Point out malaria parasites and leukocytes.
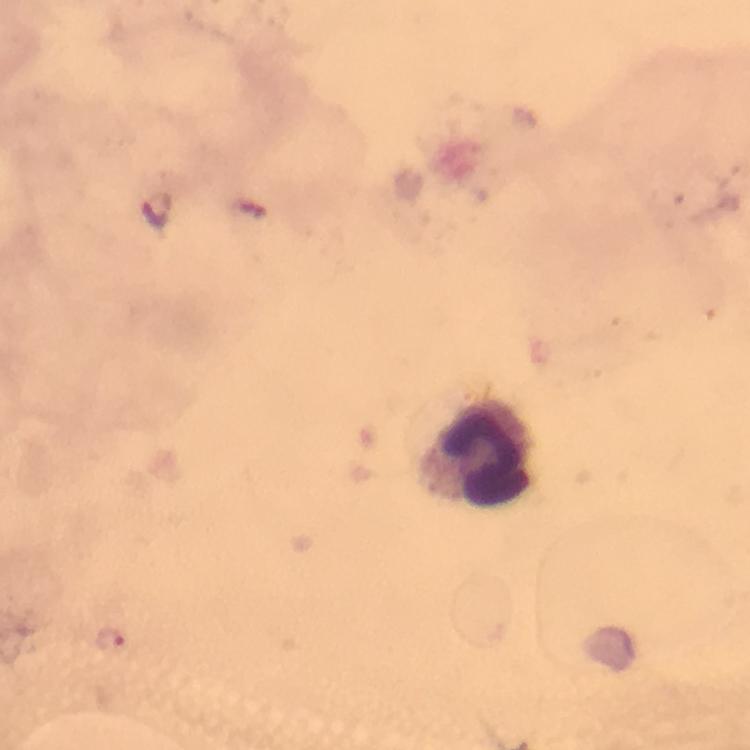

Approximate centers as [x, y] in pixels.
Malaria parasites: [107, 637].
Leukocytes: [479, 452].

Giemsa stain. From a malaria diagnostic workup. Image is 750×750 pixels. Smartphone photograph taken through a microscope. Immersion oil applied. Thick blood film. 100x magnification. A crop from one field of view.